Classify this cell by malaria status.
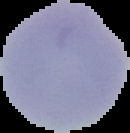
It is uninfected.

image_type: segmented cell region with the area outside set to black
preparation: thin blood smear
image_size: 130×133 pixels